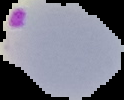
Result: malaria parasites identified. From a thin blood smear. Cell region segmented out of the field of view; the surrounding area is masked to black. Image is 124×100 pixels.